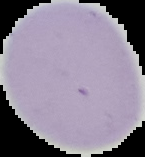

From a thin blood film. The area outside the segmented cell region is set to black. Malaria status: uninfected. Image is 145×157 pixels.